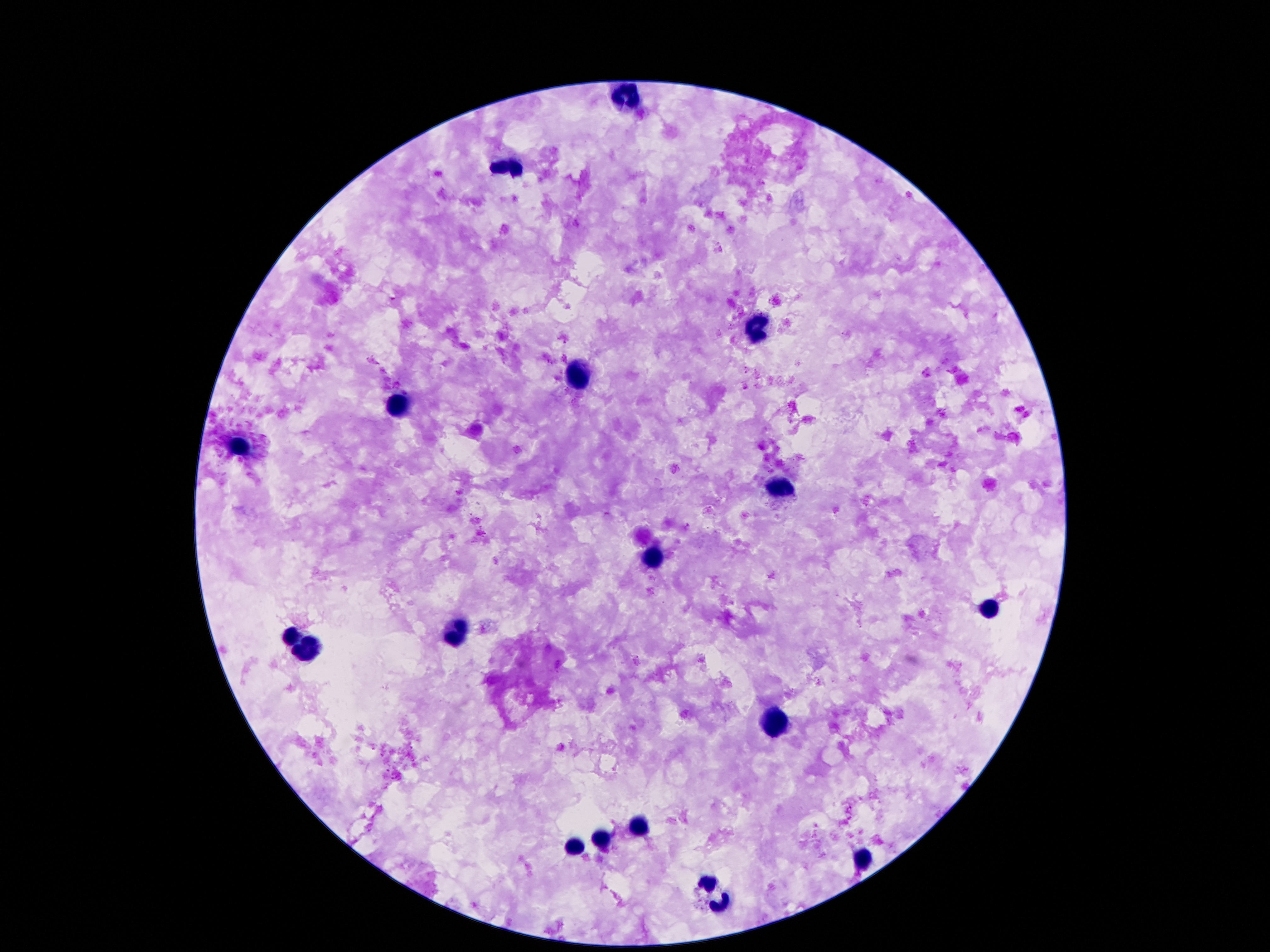
{
  "capture": "smartphone camera through the microscope eyepiece",
  "leukocyte_locations": "approximate centers as {x, y} in pixels: {631, 93}, {512, 164}, {756, 327}, {579, 375}, {402, 403}, {243, 448}, {781, 490}, {654, 561}, {990, 606}, {452, 632}, {288, 640}, {307, 651}, {775, 724}, {639, 824}, {600, 840}, {577, 848}, {865, 861}, {715, 892}",
  "magnification": "100x",
  "patient_malaria_status": "uninfected",
  "preparation": "thick peripheral-blood smear",
  "stain": "Giemsa",
  "field_of_view": "single",
  "image_size": "1270×952 pixels"
}